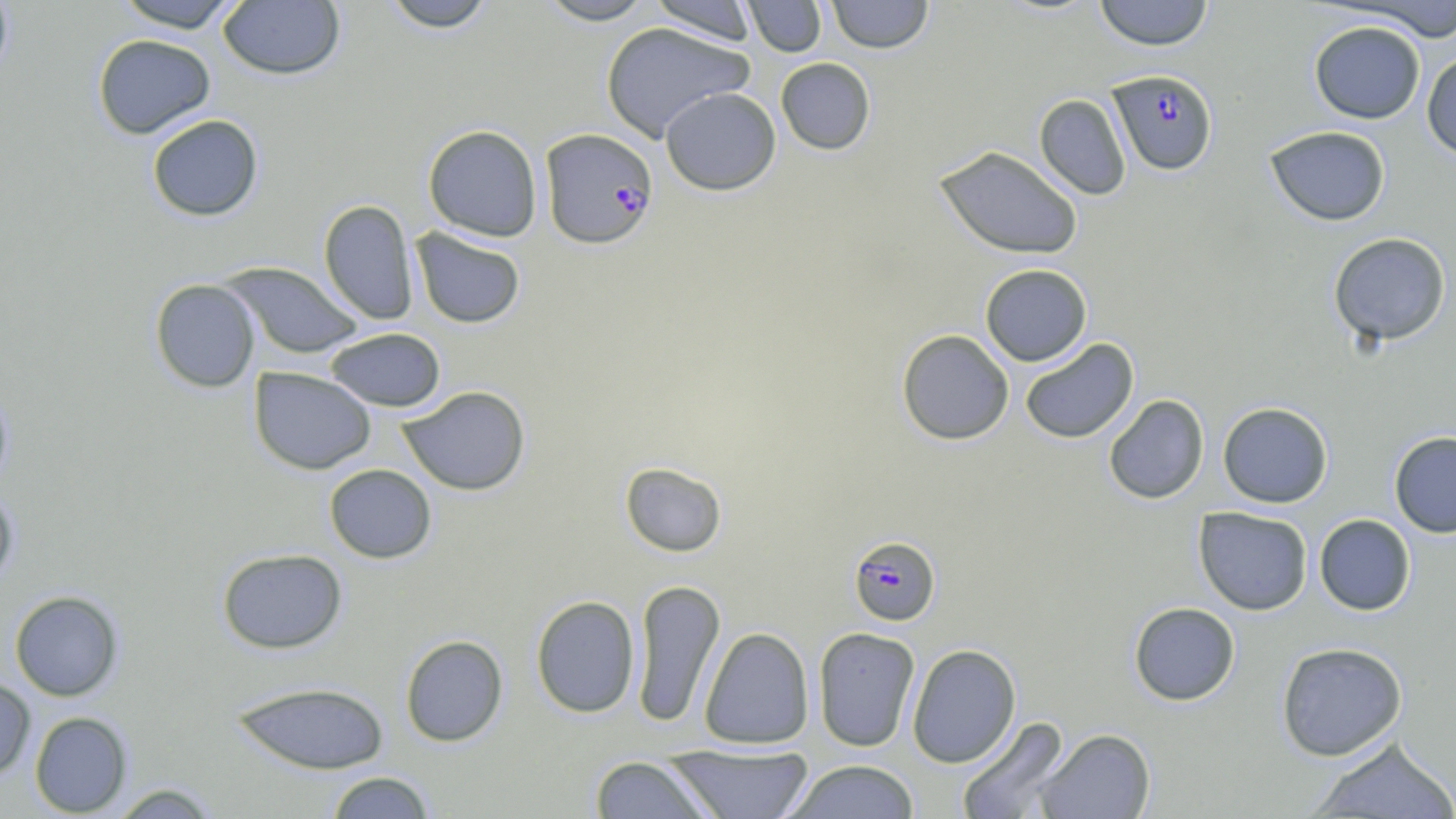

Summary:
  - Coordinate format: approximate bounding boxes as (x1,y1)-(x2,y2) corner pairs in pixels
  - Uninfected red blood cell locations: (0,0)-(16,84), (112,0)-(244,32), (379,0)-(498,32), (536,0)-(657,25), (648,0)-(759,45), (743,0)-(827,57), (825,0)-(934,53), (1093,0)-(1214,50), (217,1)-(346,80), (1351,1)-(1456,42), (1309,20)-(1425,124), (601,22)-(754,140), (92,34)-(216,140), (1421,52)-(1456,160), (775,58)-(876,155), (660,86)-(781,195), (1034,94)-(1131,200), (146,114)-(264,221), (422,124)-(543,242), (1264,125)-(1391,226), (933,145)-(1084,260), (318,199)-(419,326), (410,227)-(526,329), (1327,232)-(1451,346), (221,262)-(364,359), (980,264)-(1092,366), (149,278)-(260,392), (325,327)-(445,412), (896,329)-(1014,445), (1018,338)-(1139,444), (249,367)-(376,475), (0,380)-(15,494), (398,385)-(531,496), (1103,394)-(1209,504), (1217,401)-(1333,508), (1389,431)-(1456,538), (619,461)-(728,557), (324,464)-(437,563), (0,485)-(19,591), (1193,507)-(1313,615), (1314,513)-(1416,616), (216,547)-(348,654), (630,578)-(725,727), (9,590)-(124,701), (530,595)-(641,718), (1128,602)-(1241,706), (812,626)-(920,752), (699,627)-(814,749), (399,634)-(509,746), (1275,641)-(1408,761), (906,643)-(1021,768), (0,678)-(36,779), (229,681)-(391,774), (30,711)-(133,817), (955,716)-(1072,819), (1035,728)-(1156,818), (1307,737)-(1456,818), (663,743)-(815,818), (589,755)-(718,818), (785,760)-(920,818), (325,771)-(436,818), (107,783)-(223,818)
  - Plasmodium falciparum-infected red blood cell locations: (1109,70)-(1218,176), (539,128)-(658,250), (848,535)-(940,626)
  - Slide-level diagnosis: Plasmodium falciparum
  - Stain: May-Grünwald-Giemsa
  - Modality: optical microscopy
  - Field of view: single
  - Preparation: thin blood film
  - Magnification: 1000x
  - Image size: 1456×819 pixels